Locate every Plasmodium falciparum-infected red blood cell.
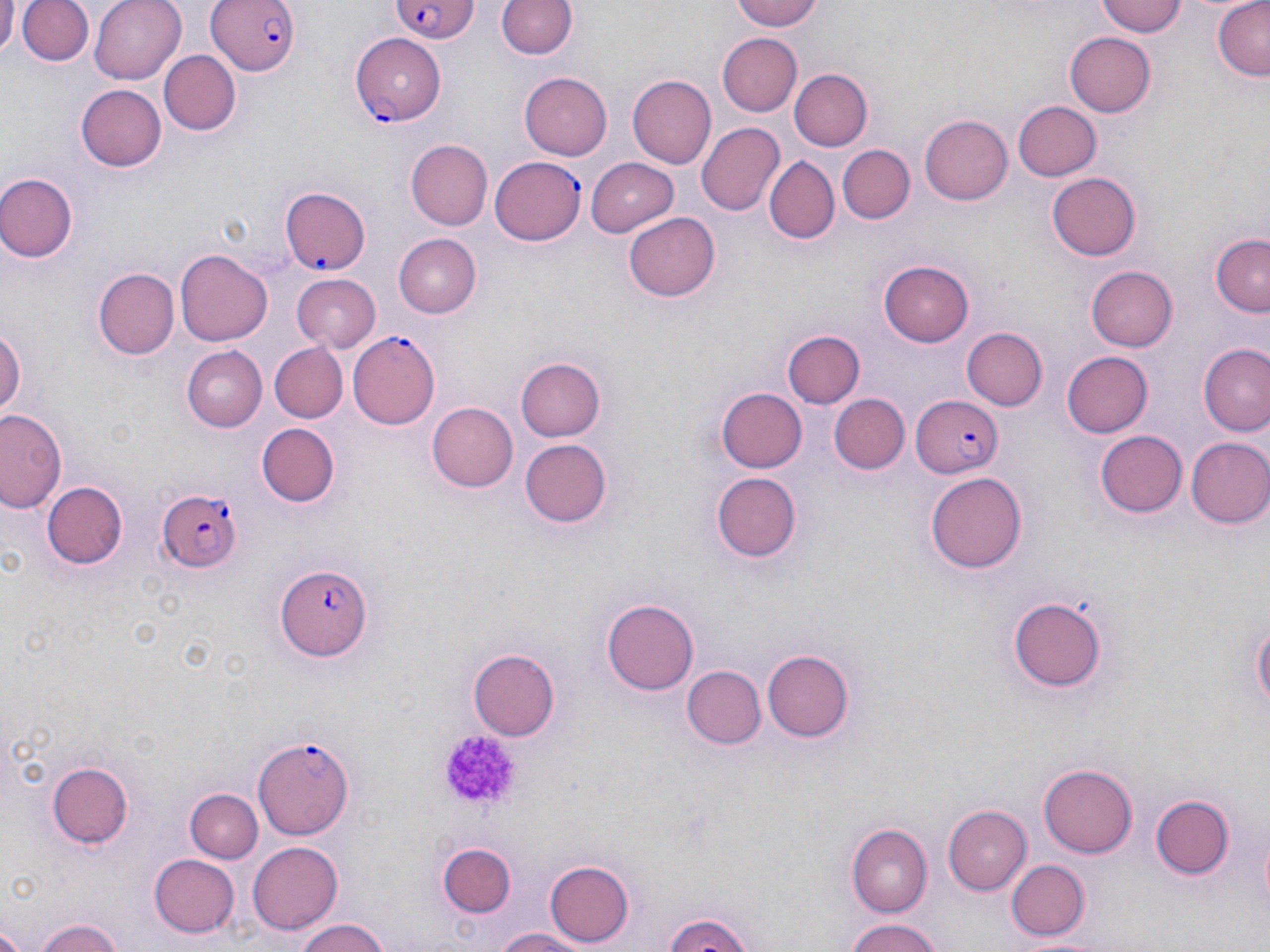
Approximate bounding boxes as [x1, y1, x2, y2] in pixels.
Plasmodium falciparum-infected red blood cells: [204, 0, 302, 77], [390, 2, 479, 47], [351, 33, 448, 122], [488, 156, 585, 247], [280, 186, 371, 276], [346, 332, 442, 429], [911, 395, 1003, 476], [154, 489, 243, 571], [275, 564, 372, 662], [253, 735, 357, 839].

Uninfected red blood cell locations: [1, 0, 18, 55], [16, 0, 94, 68], [88, 0, 185, 84], [493, 0, 578, 62], [728, 0, 826, 31], [1095, 0, 1187, 37], [1213, 0, 1269, 80], [1062, 31, 1156, 118], [715, 33, 801, 117], [158, 49, 240, 134], [789, 69, 872, 151], [519, 72, 612, 160], [628, 75, 715, 169], [75, 83, 165, 172], [1011, 100, 1101, 182], [920, 115, 1013, 206], [695, 122, 784, 216], [406, 140, 492, 230], [838, 145, 913, 224], [763, 156, 839, 245], [585, 158, 679, 237], [1047, 172, 1140, 260], [1, 173, 78, 261], [625, 212, 720, 302], [1210, 232, 1270, 318], [392, 233, 481, 317], [176, 249, 273, 347], [880, 259, 975, 345], [1088, 265, 1178, 351], [92, 268, 178, 359], [291, 274, 382, 353], [0, 324, 26, 421], [963, 327, 1048, 412], [783, 329, 864, 408], [270, 343, 347, 423], [1200, 344, 1270, 436], [184, 347, 268, 431], [1060, 351, 1152, 439], [517, 357, 605, 441], [717, 388, 806, 472], [829, 394, 908, 474], [424, 402, 521, 494], [1, 409, 67, 517], [256, 423, 336, 507], [1094, 430, 1188, 517], [1185, 437, 1270, 529], [516, 438, 613, 530], [927, 470, 1026, 570], [711, 471, 802, 564], [43, 481, 128, 568], [1006, 592, 1109, 694], [603, 598, 699, 694], [1250, 604, 1269, 723], [467, 649, 561, 741], [762, 649, 857, 741], [680, 665, 766, 749], [46, 762, 134, 850], [1039, 762, 1136, 856], [187, 788, 264, 863], [1151, 796, 1233, 879], [946, 804, 1032, 896], [845, 820, 932, 914], [247, 840, 341, 934], [438, 843, 517, 917], [150, 854, 240, 937], [546, 859, 635, 947], [1003, 859, 1089, 940], [659, 911, 758, 952], [290, 917, 395, 952], [35, 918, 126, 952], [842, 918, 948, 952], [490, 926, 597, 952], [1021, 934, 1113, 952]. Platelet locations: [436, 725, 528, 812]. Slide-level diagnosis: Plasmodium falciparum. Single field of view. Light microscopy. May-Grünwald-Giemsa-stained preparation. 1000x magnification. Image is 1270×952 pixels. Thin blood film.